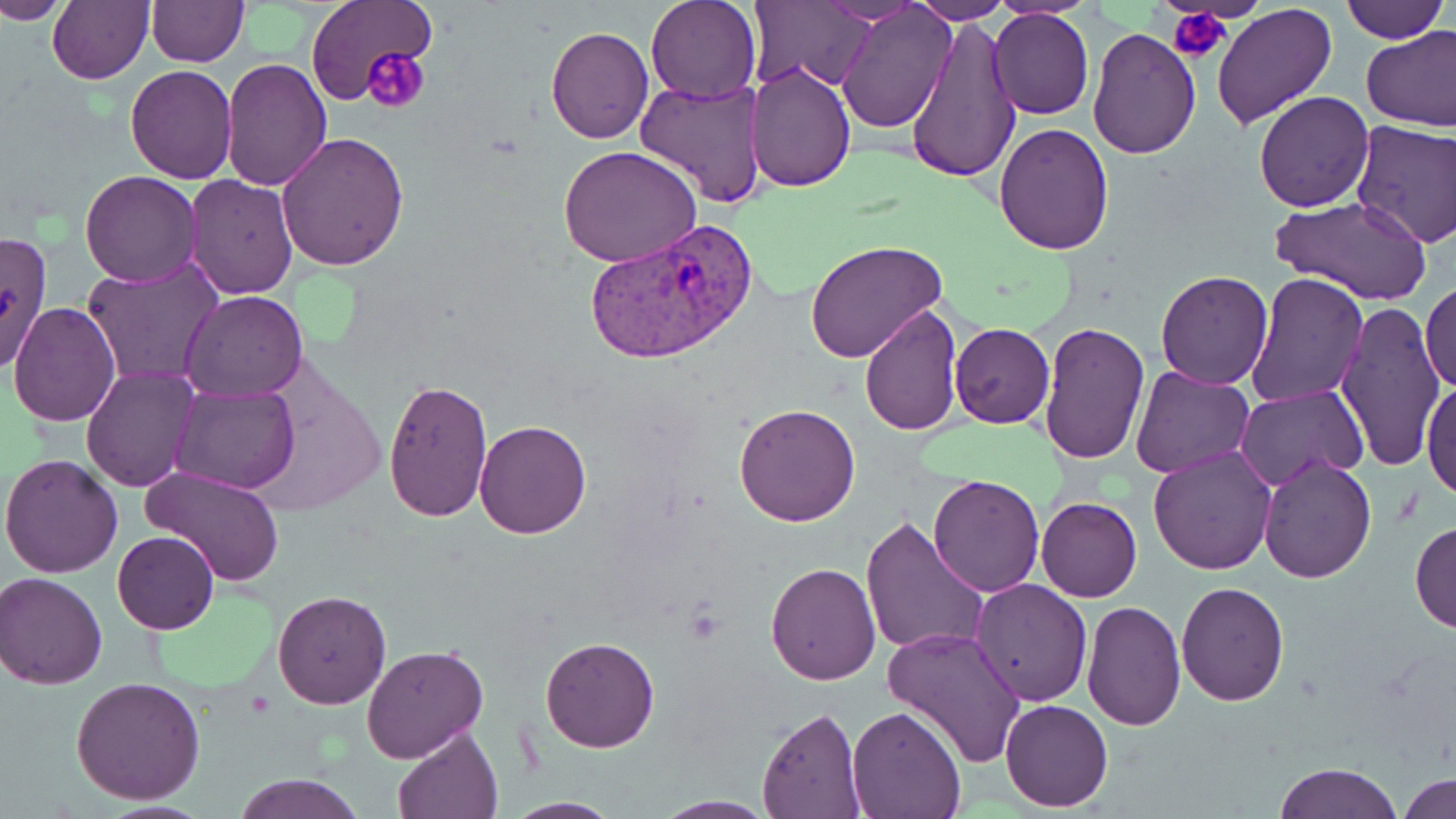

slide-level diagnosis = Plasmodium vivax
preparation = thin blood film
Plasmodium vivax-infected red blood cell locations = approximate bounding boxes as (x1, y1, x2, y2) in pixels: (585, 215, 760, 365)
stain = May-Grünwald-Giemsa
uninfected red blood cell locations = approximate bounding boxes as (x1, y1, x2, y2) in pixels: (3, 0, 66, 26), (48, 0, 155, 84), (302, 0, 435, 110), (645, 0, 761, 104), (909, 0, 1012, 23), (987, 0, 1103, 18), (1338, 0, 1448, 43), (748, 1, 878, 92), (146, 2, 248, 67), (839, 3, 956, 132), (1211, 3, 1338, 129), (988, 10, 1094, 120), (906, 13, 1021, 186), (1361, 25, 1456, 129), (546, 26, 653, 143), (1086, 26, 1201, 160), (1222, 53, 1346, 195), (221, 57, 333, 191), (746, 59, 856, 193), (125, 64, 237, 182), (636, 78, 769, 207), (1253, 90, 1374, 212), (1349, 121, 1456, 249), (994, 123, 1114, 255), (277, 130, 408, 270), (559, 145, 702, 266), (79, 170, 201, 287), (184, 174, 299, 299), (1272, 196, 1431, 307), (806, 242, 945, 361), (83, 260, 223, 387), (1155, 270, 1274, 390), (1244, 271, 1369, 410), (1420, 277, 1456, 397), (180, 290, 308, 402), (1333, 300, 1445, 472), (8, 302, 121, 428), (858, 302, 962, 437), (1038, 320, 1151, 466), (950, 323, 1055, 427), (1130, 365, 1255, 479), (80, 367, 199, 492), (1422, 376, 1455, 504), (382, 377, 492, 523), (172, 383, 297, 495), (1235, 385, 1366, 492), (733, 403, 861, 525), (475, 419, 591, 539), (1147, 445, 1276, 575), (1, 452, 124, 578), (1259, 455, 1376, 583), (141, 465, 286, 586), (928, 474, 1044, 597), (1036, 497, 1142, 602), (860, 516, 986, 657), (1409, 520, 1456, 633), (113, 531, 219, 635), (765, 562, 882, 684), (1, 571, 107, 688), (970, 578, 1091, 705), (1177, 580, 1289, 704), (272, 590, 391, 708), (1085, 594, 1283, 715), (1082, 601, 1186, 731), (882, 625, 1026, 768), (539, 638, 660, 753), (362, 645, 488, 762), (70, 676, 206, 805), (1001, 699, 1113, 813), (756, 705, 865, 819), (845, 706, 967, 819), (393, 723, 505, 818), (1273, 761, 1404, 819), (236, 772, 363, 819), (1401, 772, 1455, 818), (649, 797, 778, 819), (501, 798, 624, 818)
modality = optical microscopy
magnification = 1000x
image size = 1456×819 pixels
field of view = one of a larger specimen
platelet locations = approximate bounding boxes as (x1, y1, x2, y2) in pixels: (1168, 6, 1232, 65), (362, 46, 429, 113)